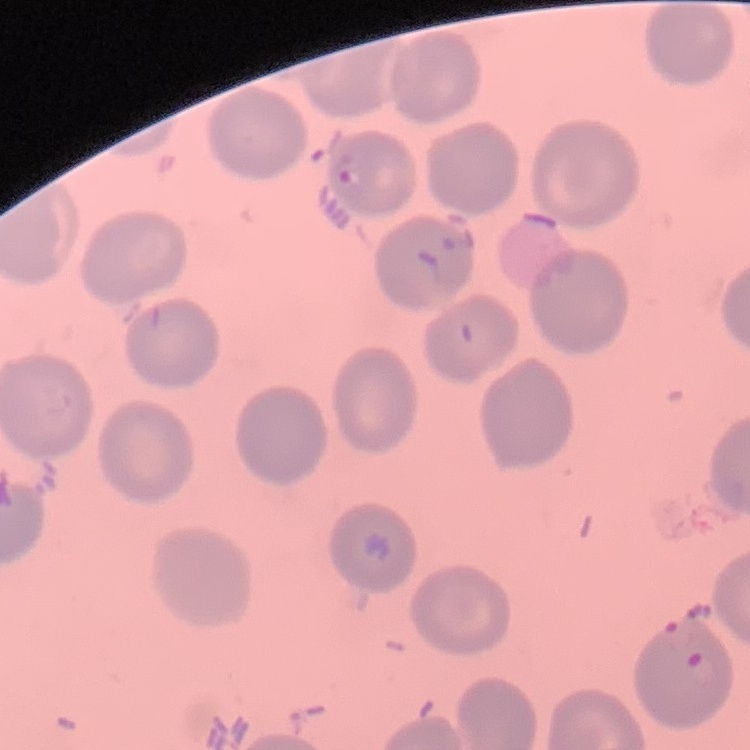
Summary:
  - Erythrocyte morphology: no rouleaux formation
  - Stain: Field's or Giemsa
  - Preparation: thin blood smear
  - Image type: one tile cut from a larger photomicrograph